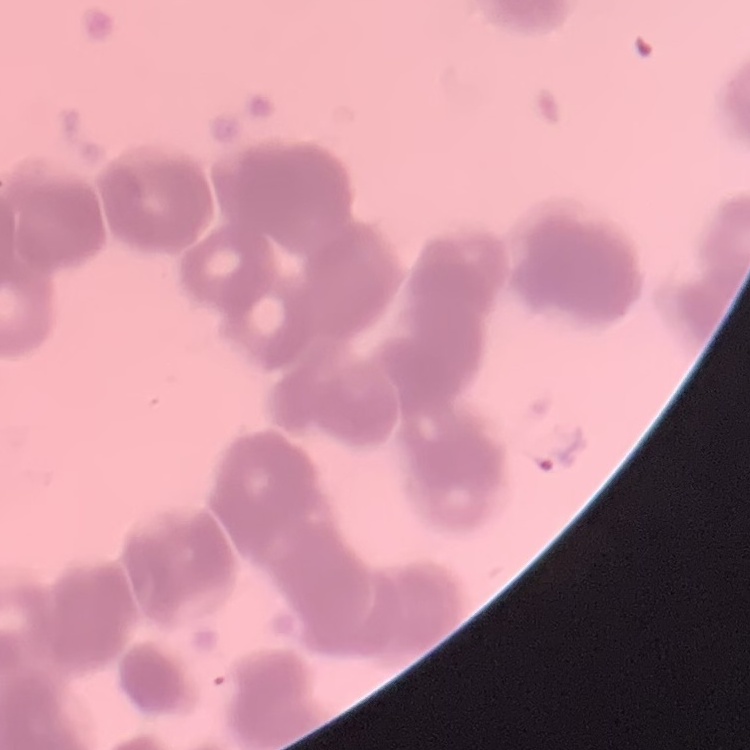

Summary:
  - Red blood cell morphology: rouleaux formation
  - Image type: one tile cut from a larger photomicrograph
  - Preparation: thin blood film
  - Stain: Field's or Giemsa